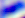 Photomicrograph. Toxoplasma gondii is shown. Captured at 400x magnification.